Name the blood parasite species.
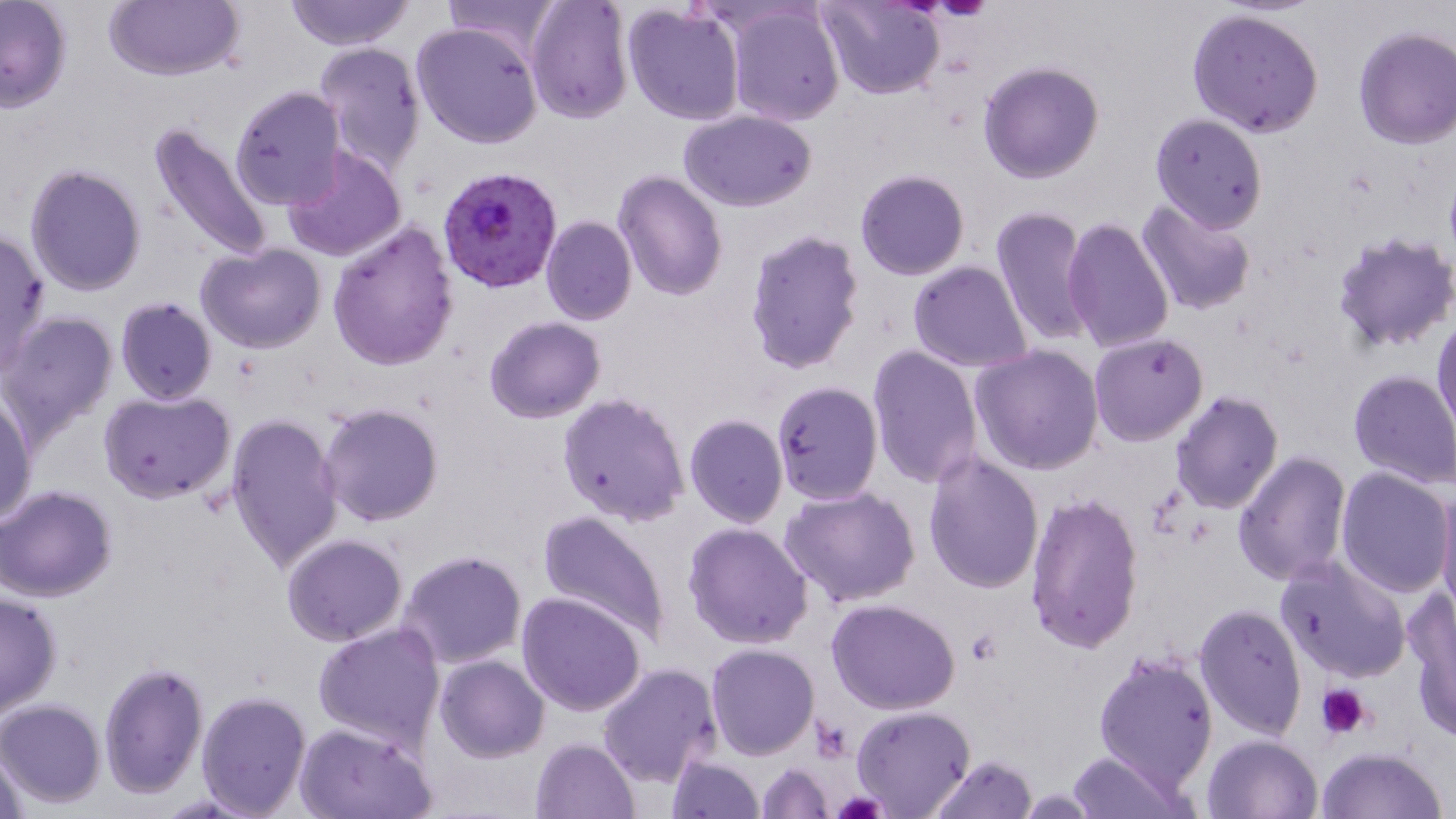

Plasmodium falciparum.

{
  "platelet_locations": "approximate bounding boxes as (x1,y1)-(x2,y2) corner pairs in pixels: (1316,683)-(1372,739), (832,793)-(888,819)",
  "magnification": "1000x",
  "plasmodium_falciparum_infected_red_blood_cell_locations": "approximate bounding boxes as (x1,y1)-(x2,y2) corner pairs in pixels: (435,166)-(562,294)",
  "image_size": "1456×819 pixels",
  "uninfected_red_blood_cell_locations": "approximate bounding boxes as (x1,y1)-(x2,y2) corner pairs in pixels: (105,0)-(243,82), (284,0)-(413,50), (440,0)-(564,62), (525,0)-(634,124), (819,0)-(945,100), (0,1)-(73,114), (622,3)-(746,127), (722,3)-(845,127), (1187,7)-(1325,138), (411,20)-(544,151), (1353,25)-(1456,150), (314,40)-(426,175), (978,61)-(1105,184), (228,85)-(345,210), (680,108)-(816,211), (1149,113)-(1269,233), (147,122)-(276,266), (281,146)-(408,262), (23,163)-(148,298), (611,169)-(727,301), (854,169)-(970,281), (1137,198)-(1256,316), (990,205)-(1095,349), (540,215)-(636,325), (1062,217)-(1176,356), (326,221)-(459,372), (0,228)-(50,374), (743,229)-(865,375), (1332,232)-(1456,355), (197,242)-(327,352), (907,261)-(1033,372), (115,297)-(218,406), (1432,308)-(1455,442), (0,311)-(118,442), (483,316)-(605,424), (1088,333)-(1208,446), (867,345)-(982,492), (971,345)-(1103,475), (1348,369)-(1456,489), (770,380)-(883,504), (98,390)-(235,504), (558,391)-(691,526), (1170,391)-(1283,514), (1,392)-(37,525), (319,403)-(444,527), (225,413)-(345,573), (684,414)-(788,527), (922,450)-(1044,594), (1232,451)-(1352,585), (1333,468)-(1453,596), (1,486)-(118,602), (780,487)-(920,609), (1437,487)-(1456,617), (1024,491)-(1144,654), (537,507)-(673,647), (684,521)-(815,649), (282,534)-(406,646), (395,550)-(527,670), (1274,554)-(1412,683), (516,591)-(647,716), (0,592)-(62,716), (1407,592)-(1456,741), (827,599)-(962,714), (1194,603)-(1308,739), (312,623)-(445,750), (705,644)-(819,760), (1093,648)-(1220,796), (435,655)-(549,762), (100,660)-(208,798), (598,663)-(723,789), (194,691)-(312,817), (0,700)-(105,808), (851,705)-(975,818), (294,720)-(435,819), (1201,734)-(1323,819), (531,738)-(640,819), (0,745)-(32,819), (1315,747)-(1446,819), (1066,749)-(1188,818), (664,754)-(765,819), (926,756)-(1038,819), (758,763)-(834,819)",
  "field_of_view": "single",
  "preparation": "thin blood film",
  "stain": "May-Grünwald-Giemsa",
  "modality": "light microscopy"
}